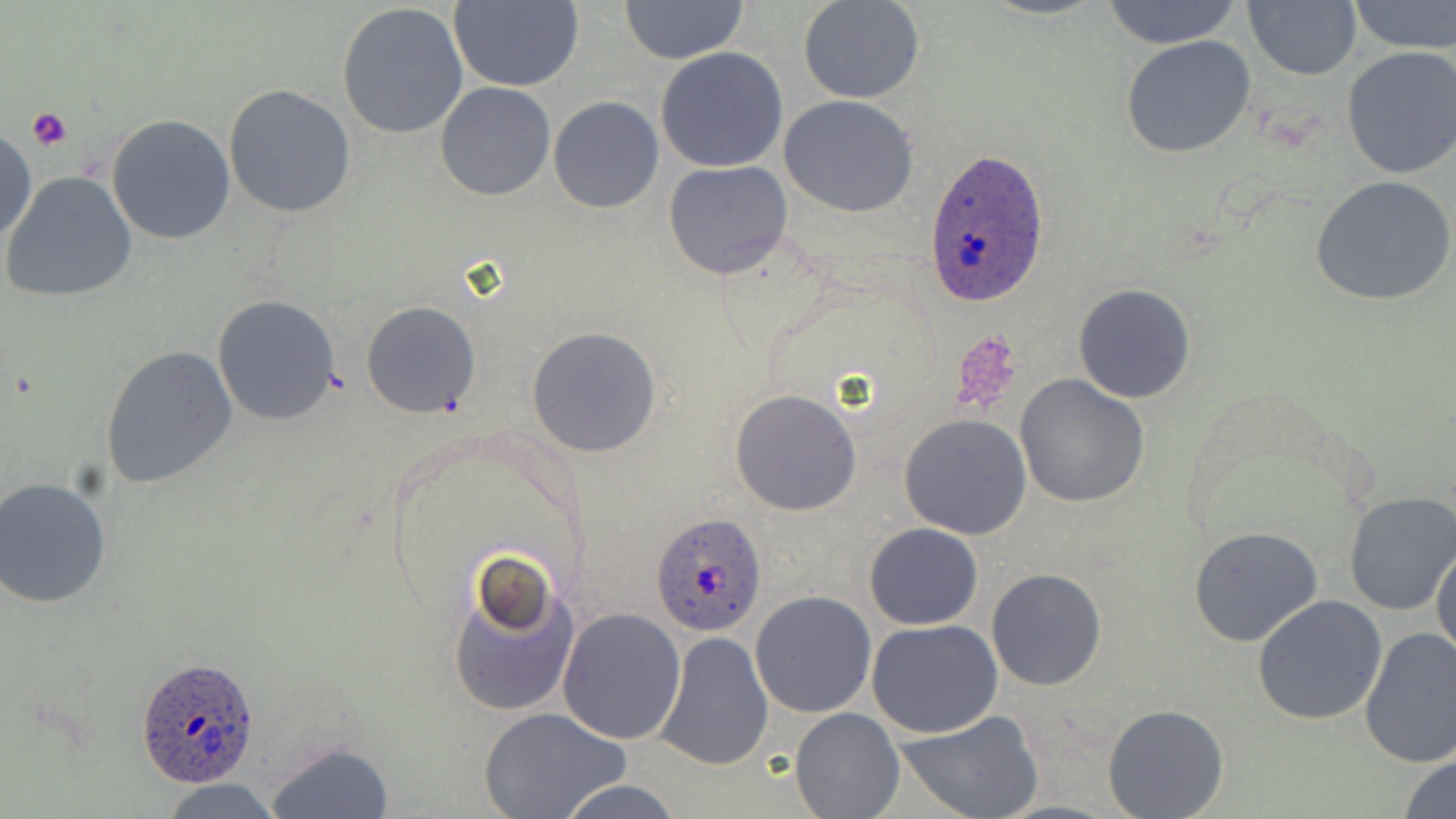

slide_level_diagnosis: Plasmodium ovale
field_of_view: single
stain: May-Grünwald-Giemsa
preparation: thin blood smear
uninfected_red_blood_cell_locations: 'approximate bounding boxes as [x1, y1, x2, y2] in pixels: [448, 0, 584, 90], [798, 0, 924, 103], [1100, 0, 1244, 49], [1244, 0, 1361, 81], [1346, 0, 1456, 54], [620, 1, 749, 65], [337, 2, 470, 140], [1120, 35, 1256, 158], [1340, 46, 1456, 181], [655, 47, 789, 173], [435, 82, 557, 201], [223, 83, 356, 218], [779, 95, 918, 217], [548, 96, 664, 214], [106, 114, 235, 245], [1, 123, 37, 248], [664, 160, 794, 281], [3, 171, 137, 303], [1310, 174, 1456, 309], [1073, 283, 1197, 404], [213, 295, 342, 426], [362, 301, 481, 418], [526, 326, 662, 458], [101, 344, 238, 491], [1015, 374, 1150, 508], [729, 388, 863, 517], [900, 412, 1033, 539], [1, 478, 115, 610], [1343, 492, 1456, 615], [864, 523, 984, 630], [1189, 526, 1324, 648], [1431, 535, 1456, 662], [447, 559, 579, 720], [987, 568, 1108, 691], [749, 591, 876, 719], [1252, 594, 1388, 725], [557, 606, 687, 744], [866, 619, 1002, 738], [1359, 627, 1456, 769], [653, 631, 774, 771], [1103, 704, 1230, 819], [790, 705, 904, 818], [481, 708, 630, 818], [894, 709, 1044, 819], [263, 739, 396, 818], [1398, 752, 1456, 819], [551, 777, 689, 819], [158, 778, 286, 818]'
platelet_locations: 'approximate bounding boxes as [x1, y1, x2, y2] in pixels: [26, 108, 72, 149], [947, 330, 1026, 415]'
plasmodium_ovale_infected_red_blood_cell_locations: 'approximate bounding boxes as [x1, y1, x2, y2] in pixels: [925, 144, 1053, 307], [651, 511, 767, 635], [137, 656, 262, 787]'
magnification: 1000x
modality: light microscopy
image_size: 1456×819 pixels